Assess the morphology of the red blood cells.
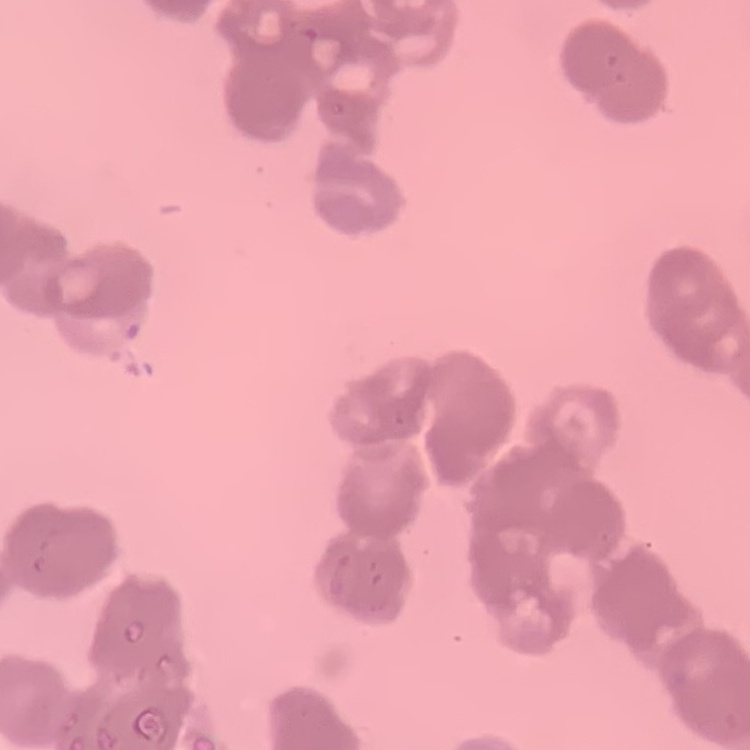

They show rouleaux formation.

Stained with either Field's or Giemsa. One tile cut from a larger photomicrograph. Thin blood film.